Locate platelets.
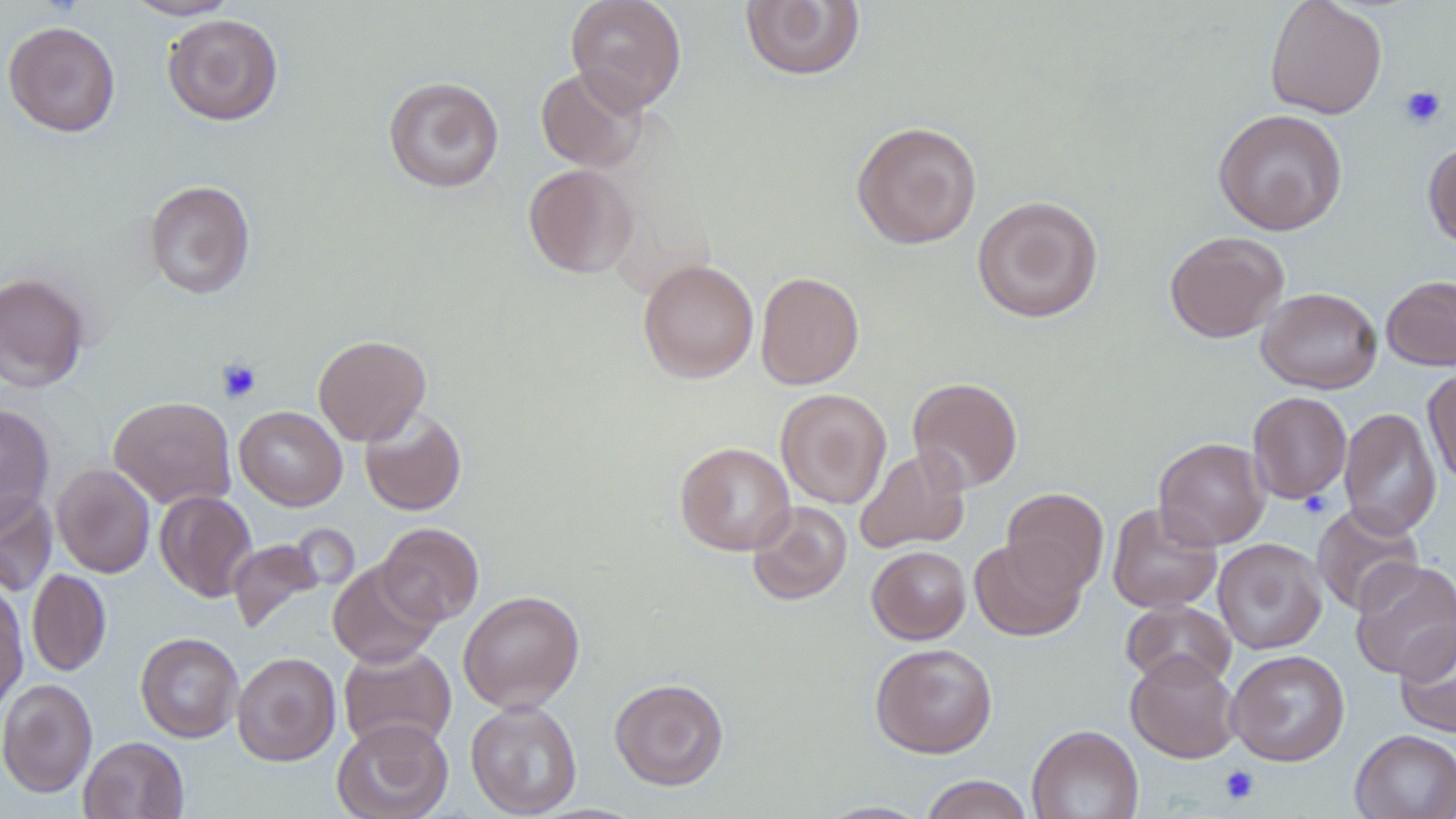

Approximate bounding boxes as named x1/y1/x2/y2 corners in pixels.
Platelets: (x1=1399, y1=85, x2=1446, y2=129), (x1=217, y1=358, x2=262, y2=404), (x1=1299, y1=491, x2=1332, y2=518), (x1=1219, y1=765, x2=1260, y2=805).

Summary:
  - Uninfected red blood cell locations: (x1=123, y1=0, x2=240, y2=20), (x1=565, y1=0, x2=687, y2=112), (x1=1265, y1=0, x2=1387, y2=119), (x1=740, y1=1, x2=866, y2=81), (x1=162, y1=14, x2=283, y2=125), (x1=4, y1=20, x2=121, y2=137), (x1=535, y1=66, x2=647, y2=173), (x1=384, y1=76, x2=504, y2=193), (x1=1213, y1=107, x2=1348, y2=235), (x1=851, y1=120, x2=983, y2=249), (x1=1423, y1=140, x2=1456, y2=249), (x1=524, y1=163, x2=638, y2=278), (x1=143, y1=180, x2=255, y2=298), (x1=972, y1=195, x2=1103, y2=324), (x1=1164, y1=230, x2=1289, y2=343), (x1=637, y1=259, x2=759, y2=383), (x1=755, y1=270, x2=865, y2=389), (x1=0, y1=271, x2=90, y2=393), (x1=1381, y1=275, x2=1456, y2=371), (x1=1256, y1=287, x2=1382, y2=394), (x1=313, y1=334, x2=431, y2=445), (x1=1422, y1=366, x2=1456, y2=488), (x1=907, y1=377, x2=1023, y2=492), (x1=775, y1=388, x2=892, y2=509), (x1=1247, y1=391, x2=1352, y2=504), (x1=108, y1=396, x2=236, y2=509), (x1=0, y1=403, x2=55, y2=527), (x1=234, y1=406, x2=347, y2=510), (x1=359, y1=407, x2=467, y2=516), (x1=1339, y1=407, x2=1442, y2=538), (x1=1153, y1=437, x2=1270, y2=550), (x1=675, y1=442, x2=796, y2=555), (x1=855, y1=446, x2=970, y2=554), (x1=52, y1=464, x2=155, y2=578), (x1=1002, y1=487, x2=1109, y2=594), (x1=155, y1=490, x2=257, y2=602), (x1=0, y1=491, x2=58, y2=596), (x1=747, y1=501, x2=852, y2=605), (x1=1107, y1=502, x2=1222, y2=613), (x1=1311, y1=503, x2=1424, y2=616), (x1=376, y1=522, x2=484, y2=626), (x1=227, y1=537, x2=325, y2=634), (x1=969, y1=537, x2=1087, y2=640), (x1=1213, y1=538, x2=1326, y2=654), (x1=867, y1=545, x2=971, y2=644), (x1=327, y1=559, x2=442, y2=668), (x1=1350, y1=559, x2=1456, y2=681), (x1=27, y1=569, x2=112, y2=676), (x1=0, y1=584, x2=28, y2=713), (x1=458, y1=590, x2=585, y2=713), (x1=1121, y1=600, x2=1236, y2=690), (x1=1395, y1=622, x2=1456, y2=738), (x1=135, y1=632, x2=244, y2=743), (x1=870, y1=642, x2=998, y2=758), (x1=338, y1=643, x2=456, y2=753), (x1=1226, y1=649, x2=1350, y2=766), (x1=1125, y1=650, x2=1241, y2=763), (x1=232, y1=651, x2=341, y2=766), (x1=609, y1=677, x2=729, y2=790), (x1=0, y1=678, x2=98, y2=798), (x1=465, y1=700, x2=582, y2=817), (x1=331, y1=718, x2=454, y2=819), (x1=1027, y1=724, x2=1143, y2=819), (x1=1350, y1=729, x2=1456, y2=819), (x1=79, y1=736, x2=189, y2=819), (x1=919, y1=775, x2=1034, y2=819)
  - Slide-level diagnosis: no evidence of blood parasites
  - Magnification: 1000x
  - Field of view: one of a larger specimen
  - Preparation: thin blood smear
  - Modality: light microscopy
  - Stain: May-Grünwald-Giemsa
  - Image size: 1456×819 pixels